Locate every Plasmodium parasite.
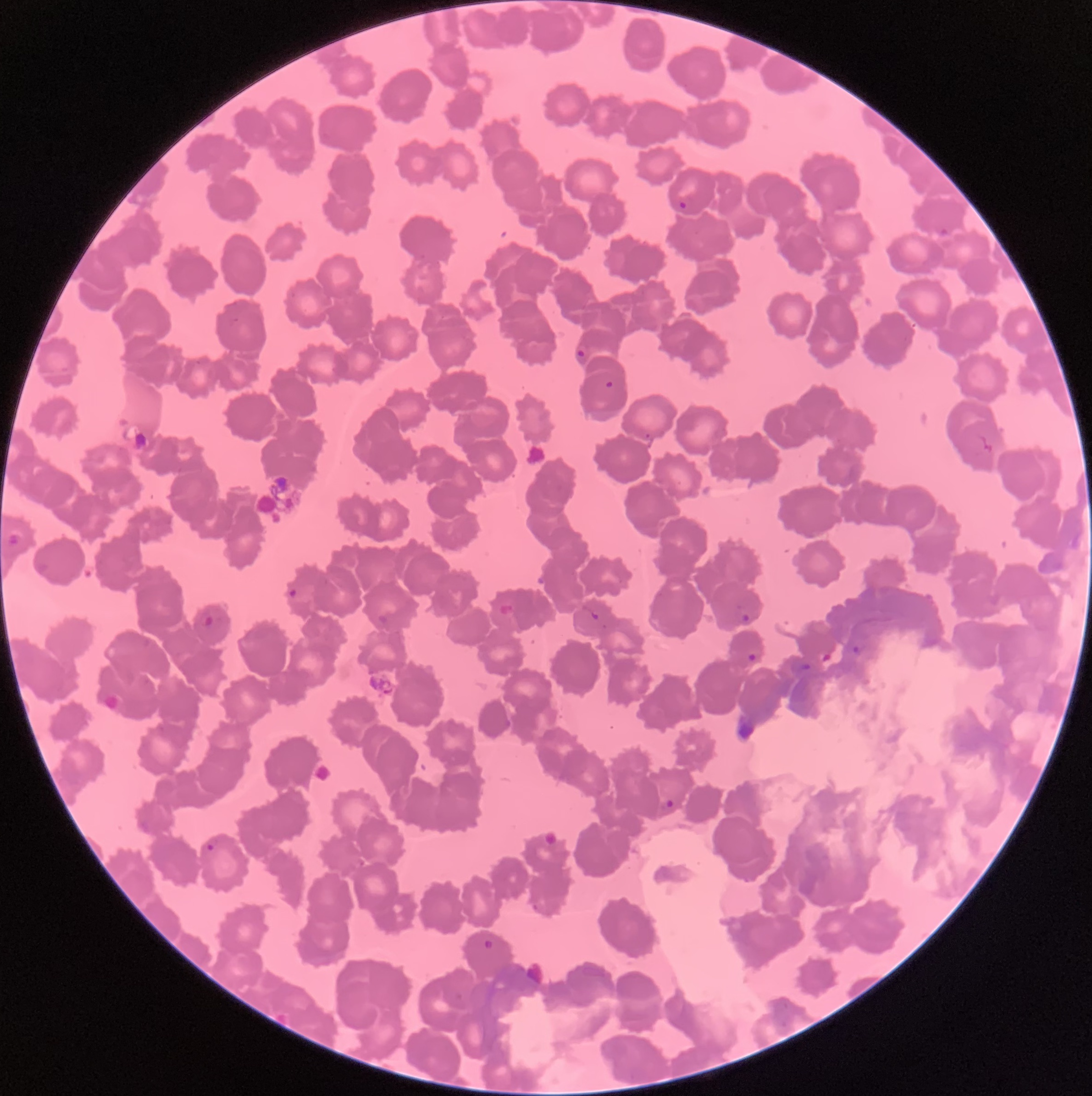
Approximate bounding boxes as named x1/y1/x2/y2 corners in pixels.
Plasmodium parasites: (x1=679, y1=200, x2=687, y2=210), (x1=936, y1=226, x2=950, y2=238), (x1=576, y1=348, x2=586, y2=358), (x1=605, y1=380, x2=614, y2=390), (x1=287, y1=587, x2=297, y2=599), (x1=589, y1=608, x2=599, y2=620), (x1=198, y1=611, x2=215, y2=627), (x1=741, y1=612, x2=751, y2=623), (x1=851, y1=645, x2=861, y2=655), (x1=746, y1=652, x2=757, y2=663), (x1=800, y1=662, x2=811, y2=670), (x1=662, y1=796, x2=679, y2=814), (x1=204, y1=836, x2=220, y2=852), (x1=530, y1=901, x2=541, y2=912), (x1=481, y1=938, x2=496, y2=952).

Summary:
  - Red blood cell morphology: rouleaux formation
  - Modality: light microscopy
  - Image size: 1092×1096 pixels
  - Preparation: thin blood film